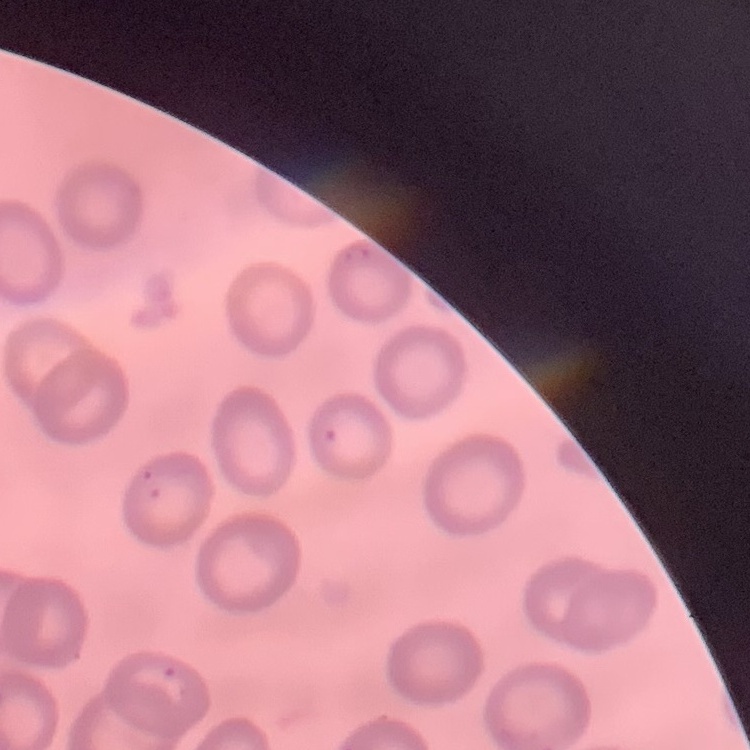

erythrocyte morphology = no rouleaux formation
stain = Field's or Giemsa
preparation = thin peripheral smear
image type = one tile cut from a larger photomicrograph